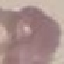

Summary:
  - Result: no malaria parasites seen
  - Image type: automatically extracted cell patch, resized to 64 × 64 pixels
  - Stain: Giemsa
  - Capture: smartphone through the microscope eyepiece
  - Preparation: thin smear